Outline each blood parasite and name the species.
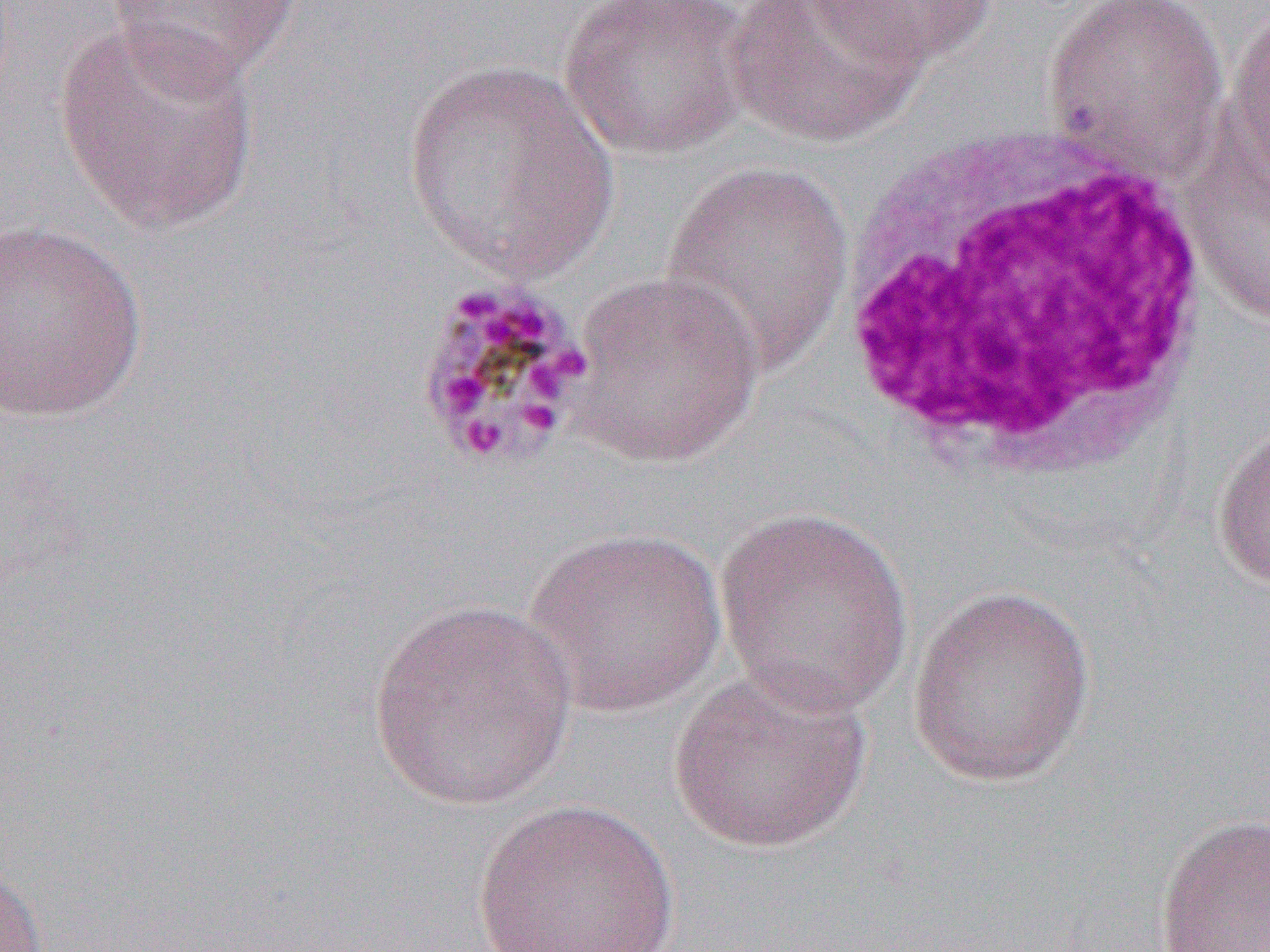
Approximate bounding boxes as (x1,y1)-(x2,y2) corner pairs in pixels.
Plasmodium malariae-infected red blood cells: (412,277)-(594,471).
No Plasmodium falciparum, Plasmodium ovale, Plasmodium vivax, Babesia divergens, or Trypanosoma brucei observed.

slide-level diagnosis = Plasmodium malariae
field of view = one of a larger specimen
modality = optical microscopy
uninfected red blood cell locations = approximate bounding boxes as (x1,y1)-(x2,y2) corner pairs in pixels: (558,0)-(752,161), (724,0)-(926,147), (1040,0)-(1230,178), (102,1)-(304,87), (805,1)-(1000,71), (1224,4)-(1269,194), (54,18)-(263,235), (400,60)-(623,284), (1183,139)-(1270,327), (659,162)-(856,374), (0,218)-(149,423), (563,270)-(766,468), (1210,421)-(1270,594), (713,505)-(916,720), (523,527)-(729,717), (906,583)-(1098,788), (364,600)-(578,810), (666,667)-(874,855), (471,798)-(681,952), (1152,811)-(1270,951), (0,862)-(49,952)
white blood cell locations = approximate bounding boxes as (x1,y1)-(x2,y2) corner pairs in pixels: (827,108)-(1235,478)
image size = 1270×952 pixels
preparation = thin blood film
magnification = 1000x